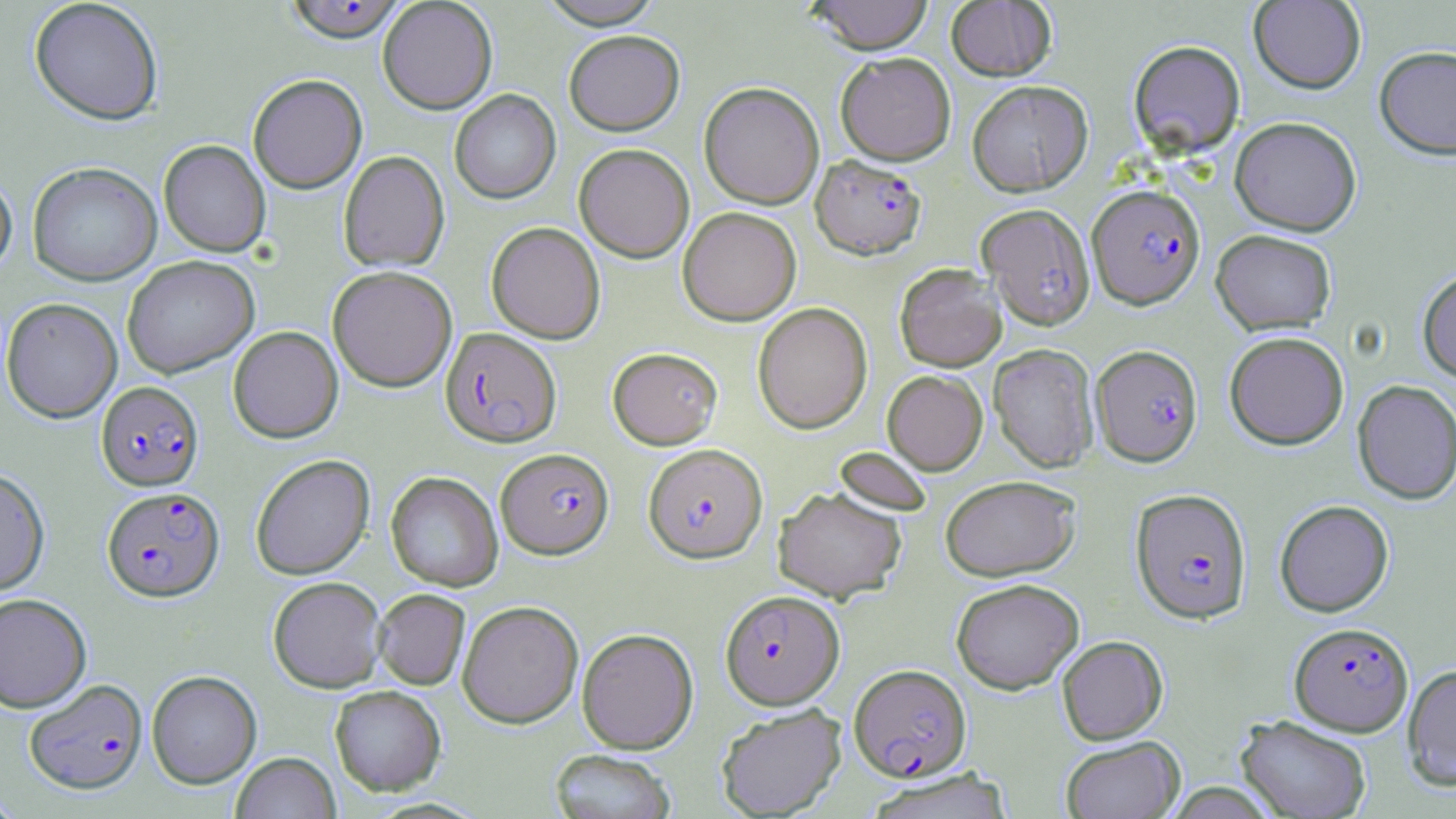 Approximate bounding boxes as (x1, y1, x2, y2) in pixels. Plasmodium falciparum-infected red blood cell locations: (284, 0, 406, 43), (810, 154, 926, 259), (1086, 184, 1205, 309), (976, 203, 1096, 330), (440, 327, 562, 447), (1090, 344, 1203, 466), (97, 381, 204, 490), (643, 443, 767, 563), (496, 448, 613, 559), (102, 486, 224, 601), (1131, 488, 1251, 623), (720, 590, 844, 709), (1289, 621, 1413, 736), (849, 664, 971, 782), (24, 678, 148, 794). Uninfected red blood cell locations: (29, 0, 164, 125), (378, 0, 497, 114), (538, 0, 664, 28), (808, 0, 933, 54), (1249, 0, 1366, 94), (946, 1, 1056, 81), (564, 29, 685, 135), (1128, 39, 1245, 157), (1374, 45, 1456, 159), (835, 51, 956, 165), (247, 73, 367, 194), (967, 80, 1093, 196), (699, 81, 824, 209), (449, 89, 561, 204), (1229, 116, 1362, 236), (158, 140, 271, 257), (574, 143, 694, 262), (338, 151, 450, 272), (27, 161, 162, 286), (0, 170, 17, 279), (677, 206, 801, 326), (486, 222, 605, 343), (1210, 229, 1337, 335), (122, 255, 259, 378), (894, 263, 1006, 371), (327, 265, 457, 392), (1417, 268, 1456, 383), (1, 297, 123, 423), (752, 302, 872, 434), (228, 326, 343, 443), (1224, 331, 1349, 450), (988, 344, 1099, 472), (607, 347, 722, 449), (882, 370, 987, 474), (1352, 379, 1456, 504), (834, 447, 933, 516), (251, 454, 374, 579), (0, 467, 50, 596), (386, 472, 502, 591), (940, 475, 1080, 580), (773, 485, 907, 602), (1274, 499, 1394, 616), (268, 576, 387, 693), (951, 578, 1084, 693), (372, 589, 470, 690), (0, 592, 92, 712), (457, 600, 583, 728), (577, 627, 698, 753), (1057, 635, 1168, 744), (1402, 664, 1456, 790), (147, 670, 262, 789), (330, 685, 446, 796), (716, 703, 847, 818), (1236, 715, 1372, 818), (1060, 736, 1185, 818), (549, 748, 676, 819), (231, 752, 341, 819), (864, 768, 1016, 819). Slide-level diagnosis: Plasmodium falciparum. 1000x magnification. Image is 1456×819 pixels. Thin blood smear. One field of a larger specimen. Optical microscopy. May-Grünwald-Giemsa stain.